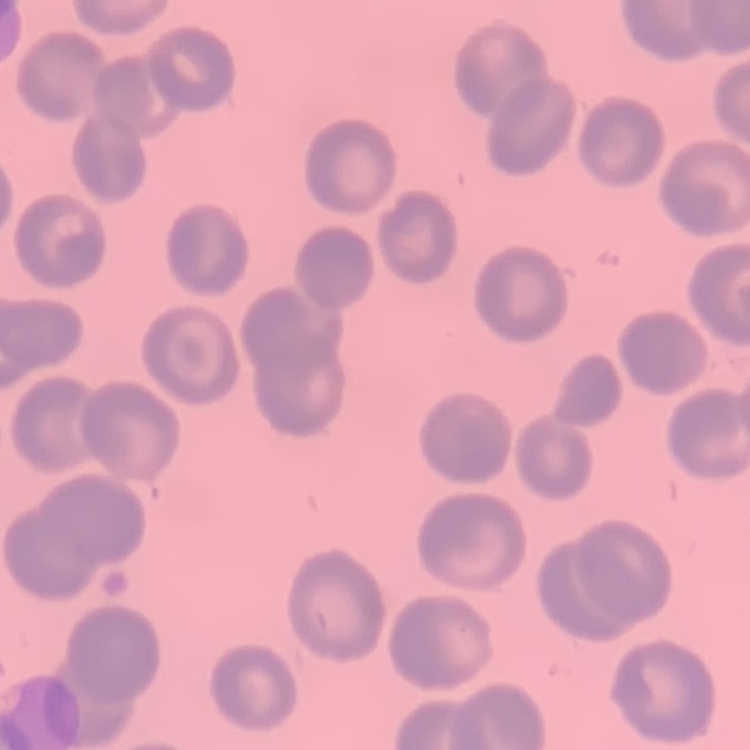
{
  "erythrocyte_morphology": "no rouleaux formation",
  "stain": "Field's or Giemsa",
  "image_type": "square crop of a larger photomicrograph",
  "preparation": "thin peripheral smear"
}